Locate every Plasmodium parasite.
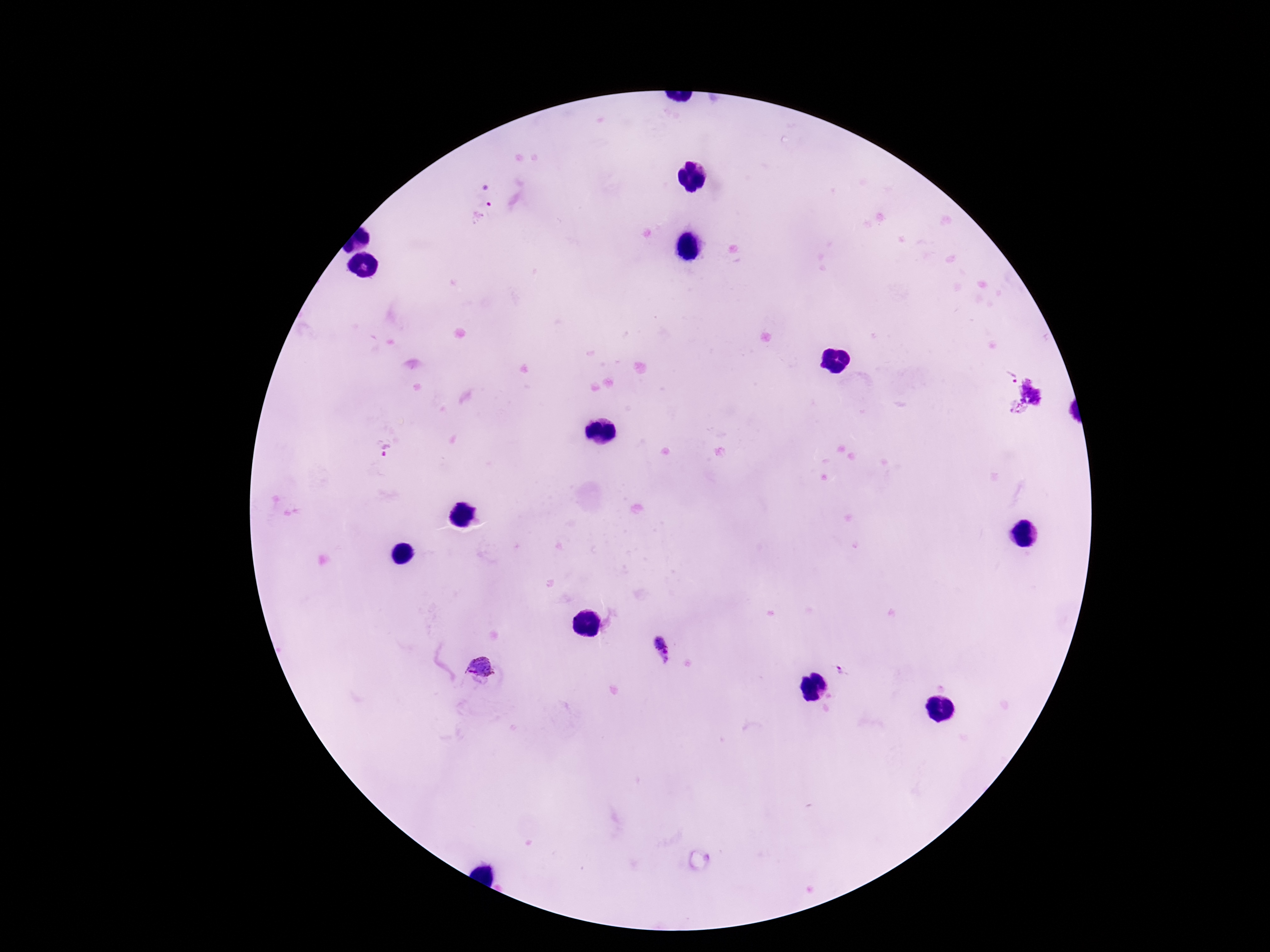
Approximate centers as {x, y} in pixels.
Plasmodium parasites: {486, 196}, {1011, 376}, {1033, 391}, {1017, 408}, {386, 450}, {661, 647}, {479, 668}, {841, 671}.

stain: Giemsa
image_size: 1270×952 pixels
field_of_view: one from this slide
magnification: 100x
capture: smartphone camera through the microscope eyepiece
patient_malaria_status: positive
preparation: thick blood smear